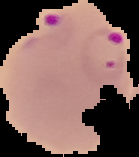
malaria status = parasitized
preparation = thin blood film
image type = segmented cell region on a black background
image size = 139×157 pixels